Name the malaria species.
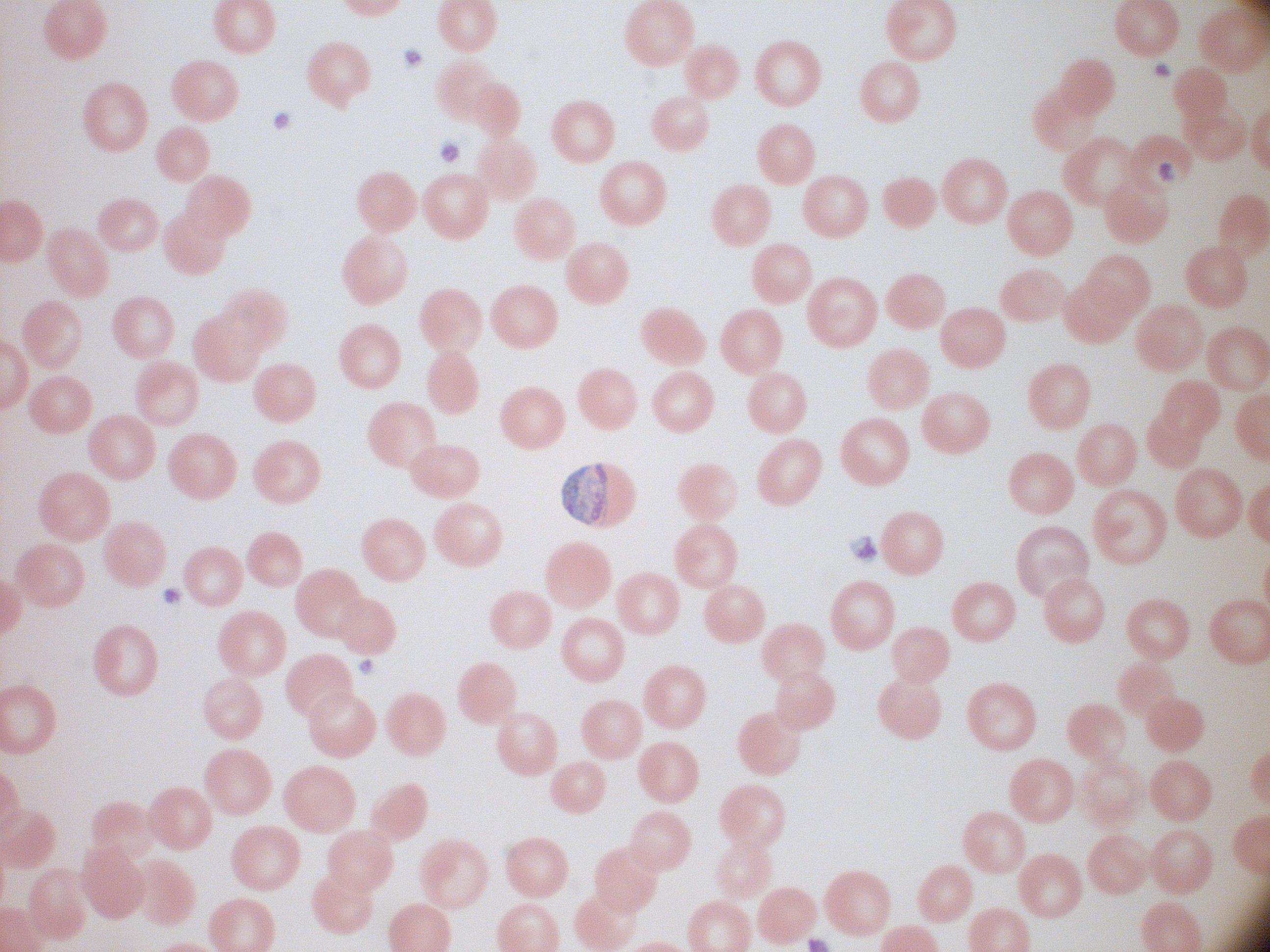
Plasmodium malariae.

Approximate bounding boxes as (x1, y1, x2, y2) in pixels, from the source annotation, which is not necessarily exhaustive. Gametocyte locations: (562, 463, 610, 529). Thin blood smear. Acquired with a Leica DM2000 optical microscope and its built-in camera. Image is 1270×952 pixels. Giemsa-stained preparation. 100x magnification. One field from this slide.